Assess this cell for malaria.
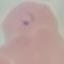
It is parasitized.

Acquired by smartphone through the microscope eyepiece. Thin smear of blood. Cell patch, automatically extracted from a larger field of view and resized to 64 × 64 pixels. Giemsa-stained preparation.